Locate every Trypanosoma brucei.
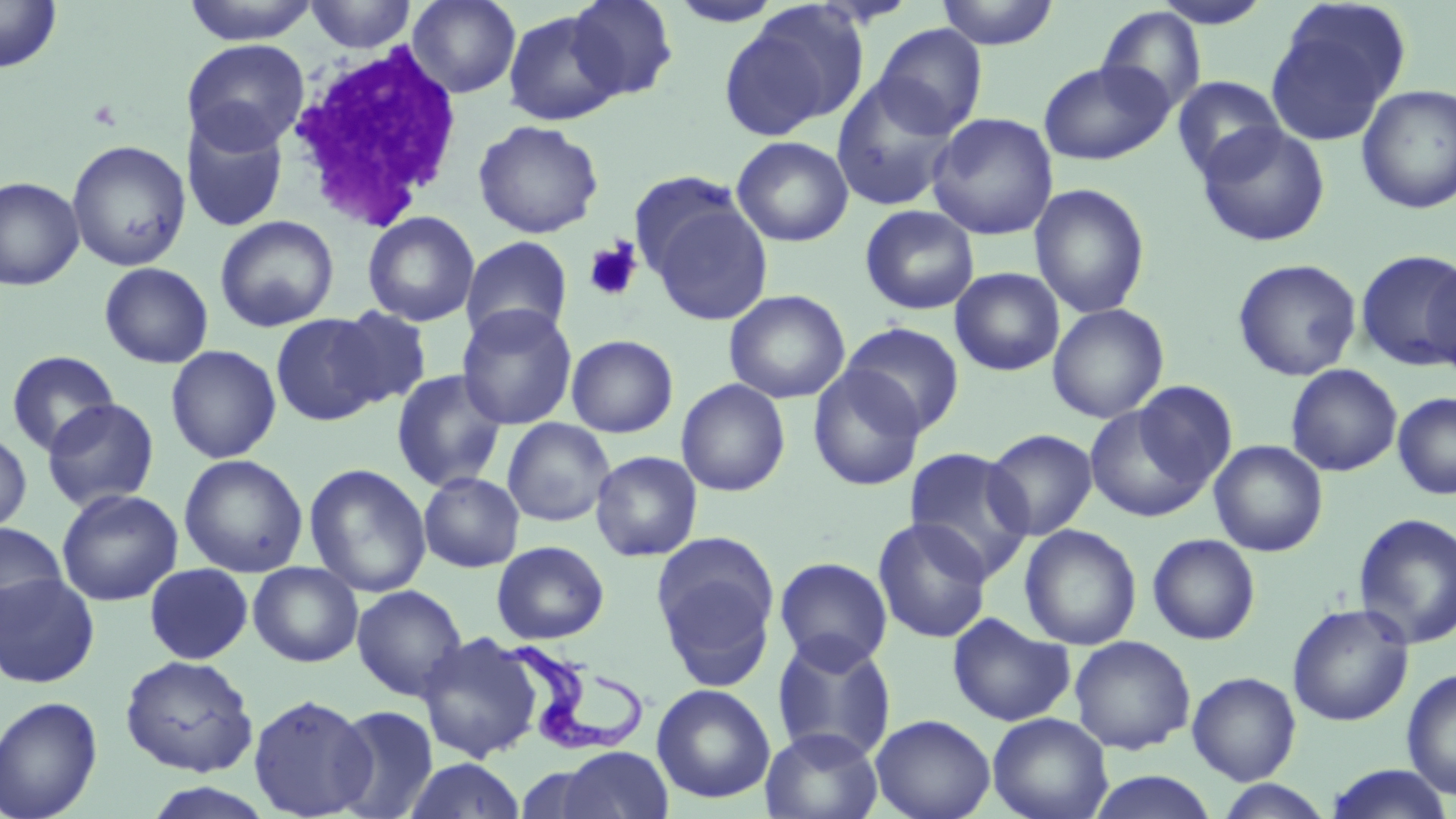

Approximate bounding boxes as (x1, y1, x2, y2) in pixels.
Trypanosoma brucei: (501, 639, 647, 754).

Platelet locations: (583, 240, 643, 302). White blood cell locations: (286, 37, 465, 231). Uninfected red blood cell locations: (0, 0, 63, 74), (181, 0, 321, 44), (406, 0, 521, 98), (565, 0, 678, 102), (935, 0, 1060, 49), (304, 1, 418, 53), (1150, 1, 1274, 29), (1267, 2, 1411, 146), (721, 4, 869, 139), (1095, 7, 1208, 115), (502, 9, 625, 126), (872, 23, 988, 138), (181, 39, 309, 153), (1038, 60, 1174, 165), (1171, 76, 1286, 182), (830, 77, 962, 212), (1356, 84, 1456, 214), (181, 112, 290, 234), (927, 112, 1058, 240), (473, 119, 604, 239), (1196, 123, 1331, 247), (731, 136, 854, 247), (66, 140, 192, 272), (627, 170, 749, 283), (0, 176, 84, 291), (1029, 183, 1151, 319), (644, 196, 774, 326), (859, 205, 979, 316), (362, 211, 480, 327), (215, 215, 339, 332), (459, 236, 574, 345), (1355, 249, 1456, 372), (1423, 257, 1456, 377), (1232, 258, 1362, 382), (99, 262, 214, 368), (950, 267, 1065, 376), (724, 289, 850, 404), (1047, 303, 1169, 424), (456, 304, 577, 431), (329, 306, 433, 408), (270, 312, 387, 427), (840, 321, 965, 436), (565, 334, 679, 438), (165, 344, 282, 464), (5, 350, 119, 457), (1285, 363, 1402, 477), (807, 365, 926, 492), (390, 369, 508, 492), (676, 379, 791, 497), (1131, 381, 1238, 492), (1392, 392, 1456, 500), (41, 398, 160, 512), (1084, 402, 1218, 524), (501, 418, 615, 527), (983, 428, 1099, 540), (0, 429, 32, 536), (1209, 440, 1328, 557), (902, 446, 1033, 580), (590, 450, 702, 562), (178, 453, 308, 578), (303, 463, 432, 598), (418, 472, 524, 573), (56, 488, 183, 606), (1352, 512, 1456, 650), (872, 517, 993, 644), (0, 521, 68, 630), (1019, 524, 1142, 651), (1146, 533, 1261, 645), (652, 535, 780, 686), (492, 540, 610, 645), (774, 556, 893, 671), (247, 561, 363, 667), (144, 563, 254, 665), (0, 571, 100, 688), (351, 584, 468, 701), (1287, 603, 1414, 727), (947, 613, 1075, 727), (417, 632, 545, 762), (771, 633, 896, 762), (1069, 635, 1196, 754), (119, 654, 258, 776), (1401, 668, 1456, 800), (1187, 671, 1301, 784), (651, 683, 776, 804), (248, 693, 376, 817), (0, 695, 104, 819), (329, 704, 439, 819), (987, 712, 1113, 819), (870, 714, 996, 819), (761, 727, 883, 819), (556, 746, 673, 819), (403, 758, 526, 818), (1324, 764, 1455, 819), (1085, 770, 1220, 818), (140, 780, 279, 819), (1214, 780, 1334, 818). Slide-level diagnosis: Trypanosoma brucei. Captured at 1000x magnification. One field of a larger specimen. May-Grünwald-Giemsa stain. Thin blood smear. Image is 1456×819 pixels. Optical microscopy.